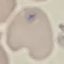

result = negative for malaria parasites
capture = smartphone through the microscope eyepiece
image type = automatically extracted cell patch, resized to 64 × 64 pixels
stain = Giemsa
preparation = thin smear